Locate every leukocyte (white blood cell).
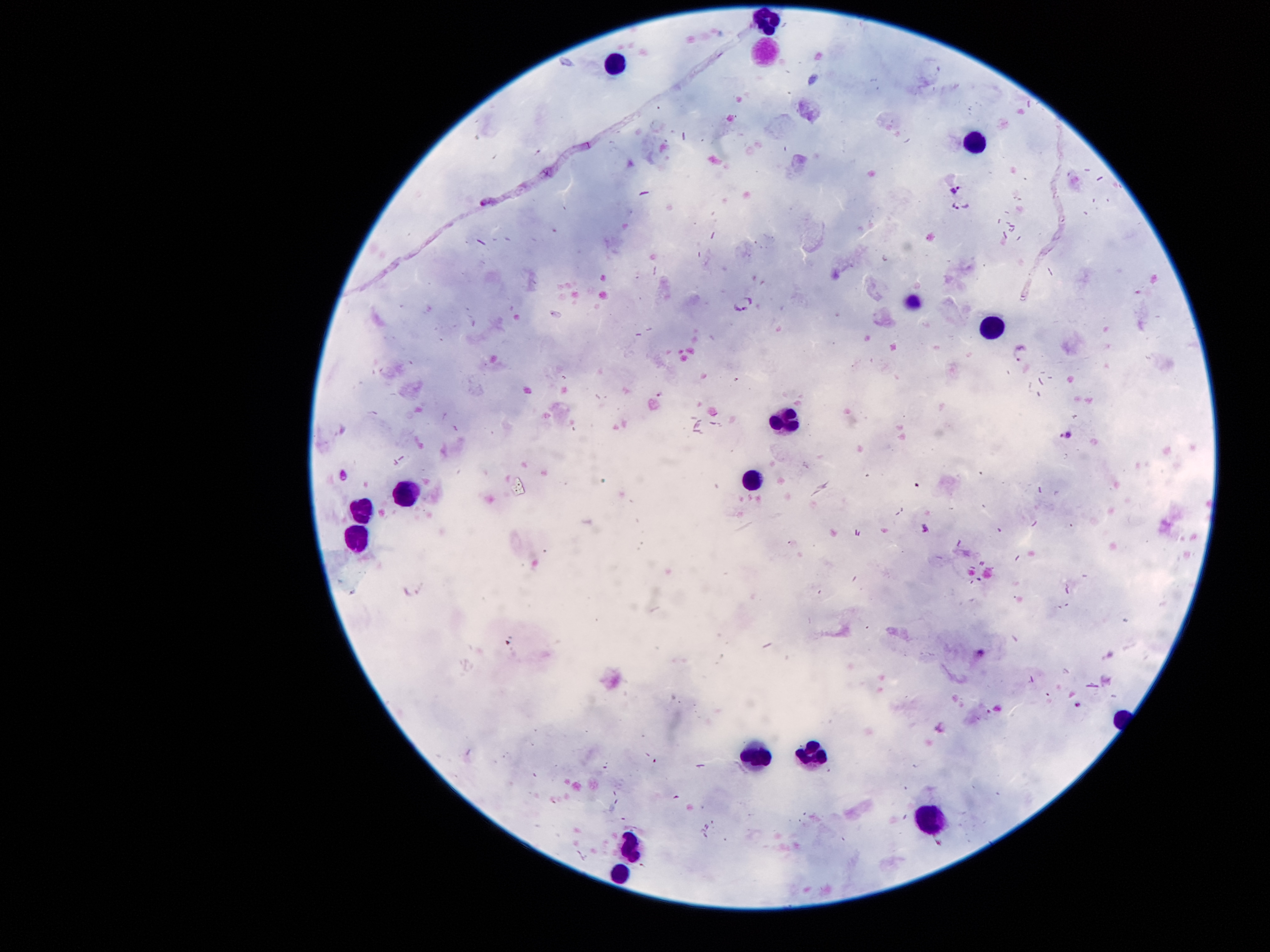

Approximate centers as {x, y} in pixels.
Leukocytes: {768, 20}, {761, 46}, {611, 63}, {971, 139}, {912, 300}, {989, 326}, {782, 417}, {754, 473}, {404, 494}, {358, 508}, {348, 549}, {810, 753}, {758, 755}, {929, 822}, {632, 847}, {618, 875}.

Summary:
  - Malaria parasite locations: {955, 189}, {485, 202}, {961, 205}, {743, 299}, {1020, 352}, {1067, 435}, {345, 474}, {982, 654}
  - Magnification: 100x
  - Preparation: thick blood film
  - Stain: Giemsa
  - Field of view: single
  - Patient malaria status: positive for Plasmodium falciparum
  - Image size: 1270×952 pixels
  - Capture: smartphone through the microscope eyepiece